Report the malaria status of this cell.
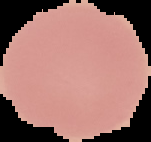

Uninfected.

preparation = thin blood film
image type = segmented cell region with the area outside set to black
image size = 151×142 pixels